Locate every blood parasite and identify its species.
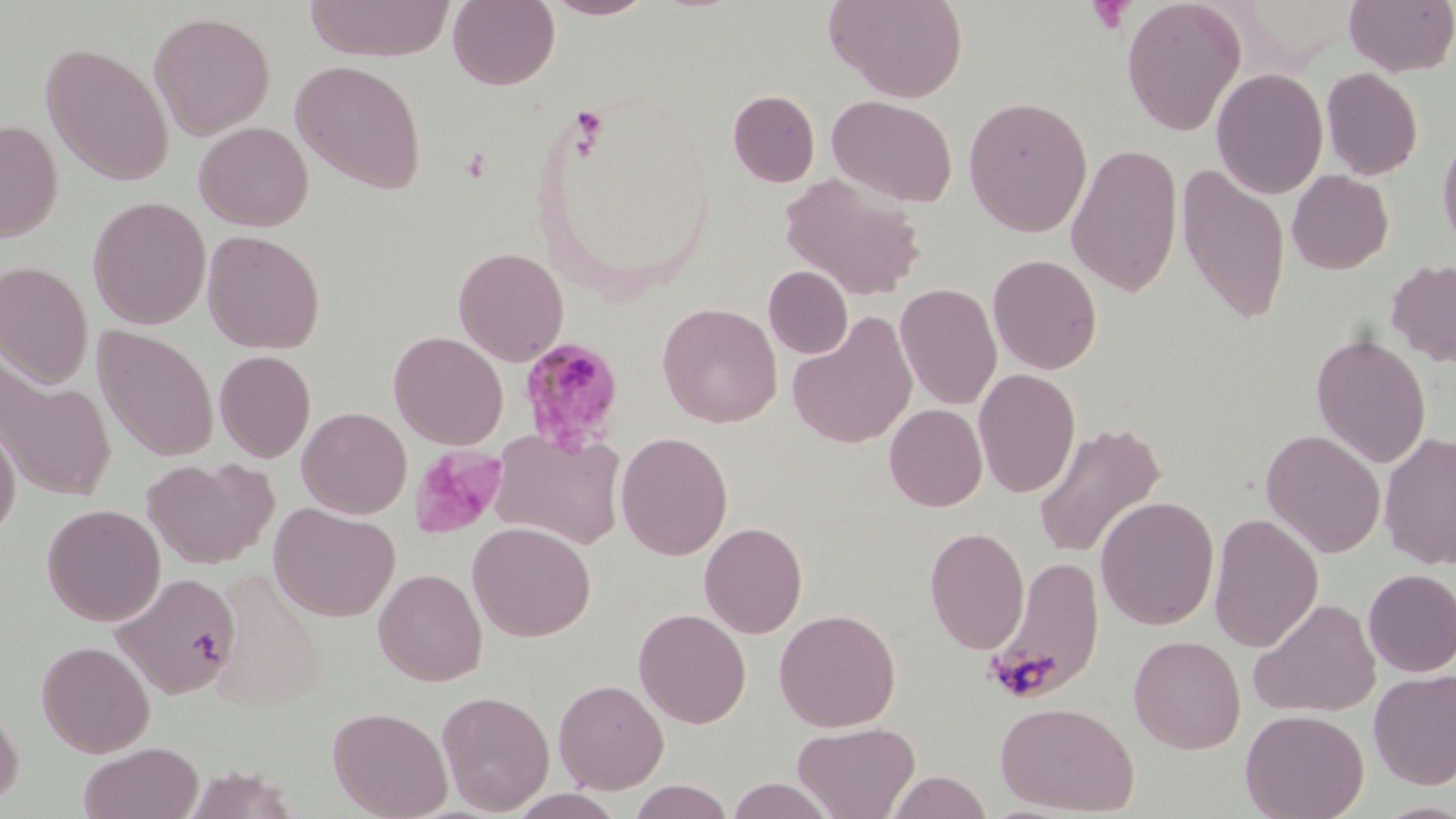
Approximate bounding boxes as (x1,y1)-(x2,y2) corner pairs in pixels.
Plasmodium malariae-infected red blood cells: (517,337)-(626,457).
No Plasmodium falciparum, Plasmodium ovale, Plasmodium vivax, Babesia divergens, or Trypanosoma brucei observed.

slide-level diagnosis = Plasmodium malariae
image size = 1456×819 pixels
field of view = single
magnification = 1000x
stain = May-Grünwald-Giemsa
platelet locations = approximate bounding boxes as (x1,y1)-(x2,y2) corner pairs in pixels: (1087,1)-(1134,35), (409,445)-(507,539)
uninfected red blood cell locations = approximate bounding boxes as (x1,y1)-(x2,y2) corner pairs in pixels: (303,0)-(454,61), (448,0)-(560,90), (543,0)-(657,19), (824,0)-(969,102), (1121,0)-(1246,136), (1343,0)-(1456,76), (148,10)-(276,141), (40,43)-(175,186), (290,60)-(427,193), (1320,67)-(1423,181), (1211,68)-(1329,199), (728,90)-(820,187), (827,94)-(958,208), (963,96)-(1093,237), (0,119)-(63,243), (193,121)-(313,232), (1437,129)-(1456,254), (1066,143)-(1183,297), (1176,163)-(1291,325), (1287,170)-(1393,274), (780,172)-(927,300), (87,195)-(211,329), (202,230)-(325,354), (453,246)-(569,366), (987,253)-(1102,374), (1386,259)-(1456,368), (0,260)-(94,388), (764,266)-(852,359), (895,282)-(1002,411), (657,302)-(782,427), (787,310)-(918,449), (93,325)-(219,461), (388,331)-(509,450), (1311,332)-(1431,468), (214,350)-(316,462), (0,360)-(116,502), (973,368)-(1080,497), (884,403)-(987,511), (297,406)-(412,519), (0,413)-(21,543), (1032,422)-(1167,559), (489,427)-(628,550), (1261,429)-(1386,558), (615,431)-(733,560), (1379,431)-(1456,569), (142,456)-(278,570), (1095,496)-(1220,630), (42,503)-(166,626), (268,503)-(401,622), (1208,512)-(1324,652), (467,521)-(595,642), (699,522)-(807,638), (924,526)-(1030,654), (987,556)-(1105,701), (373,568)-(488,686), (1362,568)-(1456,676), (113,571)-(242,700), (209,571)-(326,711), (1250,598)-(1381,718), (633,607)-(751,728), (774,608)-(900,732), (1129,635)-(1245,753), (36,639)-(155,757), (1369,669)-(1456,790), (553,678)-(669,794), (437,689)-(554,814), (0,694)-(24,810), (995,700)-(1140,815), (328,705)-(453,819), (1240,708)-(1370,819), (792,720)-(920,819), (78,741)-(204,819), (181,765)-(300,819), (885,770)-(993,818), (727,777)-(836,818), (627,780)-(734,818), (507,789)-(626,819)
preparation = thin blood film
modality = optical microscopy